Give the position of every malaria parasite.
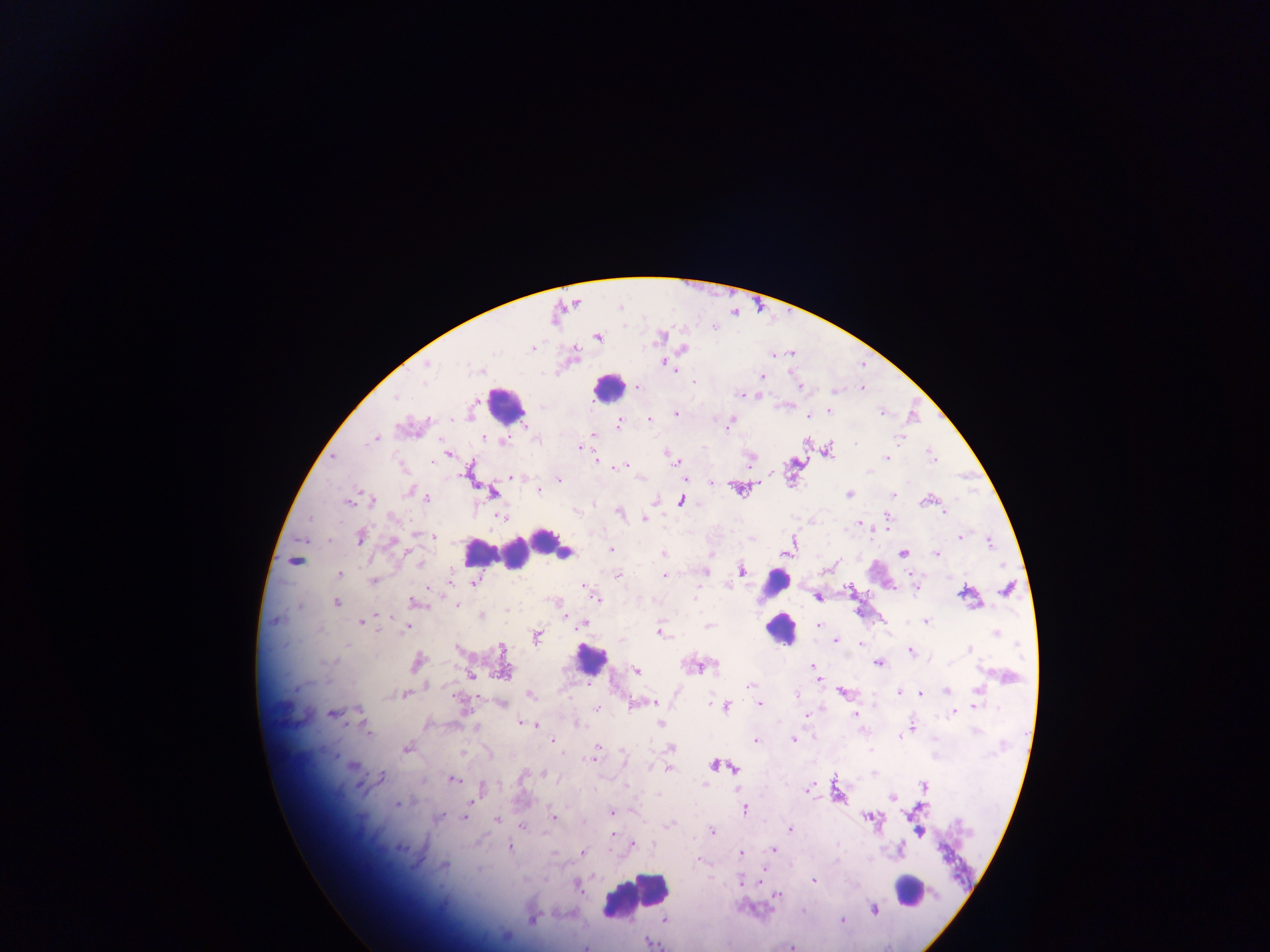
Approximate centers as (x, y) in pixels.
Malaria parasites: (597, 337), (681, 348), (790, 353), (773, 354), (662, 362), (761, 377), (636, 386), (798, 386), (861, 387), (836, 391), (741, 395), (828, 410), (676, 413), (807, 415), (648, 418), (619, 422), (728, 422), (592, 434), (375, 438), (900, 438), (580, 447), (826, 449), (447, 453), (887, 457), (748, 458), (597, 460), (675, 461), (624, 466), (772, 474), (512, 477), (559, 480), (712, 481), (740, 489), (538, 490), (410, 492), (491, 492), (849, 494), (892, 494), (426, 497), (369, 499), (929, 499), (348, 500), (680, 501), (945, 511), (618, 512), (501, 516), (644, 519), (886, 521), (861, 522), (433, 535), (359, 536), (959, 536), (990, 542), (391, 544), (790, 548), (610, 550), (902, 552), (664, 553), (710, 553), (936, 553), (295, 560), (704, 571), (740, 571), (338, 575), (618, 575), (913, 575), (664, 576), (449, 580), (372, 581), (475, 581), (583, 585), (1008, 588), (850, 591), (966, 594), (818, 596), (595, 597), (336, 602), (416, 602), (457, 605), (480, 615), (275, 620), (362, 622), (926, 622), (582, 624), (709, 624), (819, 625), (407, 626), (659, 632), (536, 636), (837, 639), (861, 645), (457, 649), (970, 649), (910, 651), (417, 662), (877, 662), (695, 665), (813, 665), (504, 669), (635, 670), (470, 676), (819, 679), (751, 684), (947, 691), (842, 692), (900, 692), (920, 693), (405, 694), (529, 694), (796, 694), (654, 703), (759, 703), (502, 704), (632, 704), (726, 706), (974, 706), (598, 708), (953, 710), (332, 712), (805, 715), (855, 715), (522, 723), (576, 723), (532, 724), (661, 725), (910, 728), (755, 740), (793, 740), (552, 741), (670, 747), (407, 748), (463, 753), (594, 758), (715, 764), (352, 765), (667, 768), (734, 769), (543, 773), (874, 773), (381, 777), (452, 779), (924, 787), (807, 788), (481, 789), (837, 791), (892, 797), (397, 803), (744, 809), (612, 812), (439, 817), (463, 817), (869, 817), (496, 819), (554, 819), (522, 828), (790, 828), (711, 831), (919, 831), (611, 834), (632, 845), (509, 847), (773, 850), (899, 850), (582, 851), (741, 853), (698, 861), (445, 865), (760, 880), (813, 880), (741, 881), (576, 884), (778, 894), (874, 909), (533, 918), (842, 919), (664, 920), (649, 942), (586, 946), (789, 946).

field of view = single
image size = 1270×952 pixels
country = Ghana
capture = mobile-phone photograph through a microscope
leukocyte locations = approximate centers as (x, y) in pixels: (609, 387), (504, 404), (544, 541), (523, 550), (480, 551), (500, 551), (563, 551), (776, 582), (781, 628), (590, 659), (908, 890), (635, 893)
preparation = thick blood film